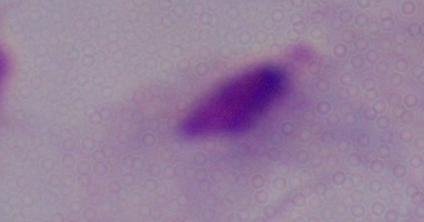

identification = trichomonad
magnification = 1000x
modality = photomicrograph